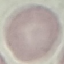
result = no malaria parasites seen
preparation = thin smear
stain = Giemsa
image type = cell patch, automatically extracted from a larger field of view and resized to 64 × 64 pixels
capture = smartphone camera at the microscope eyepiece